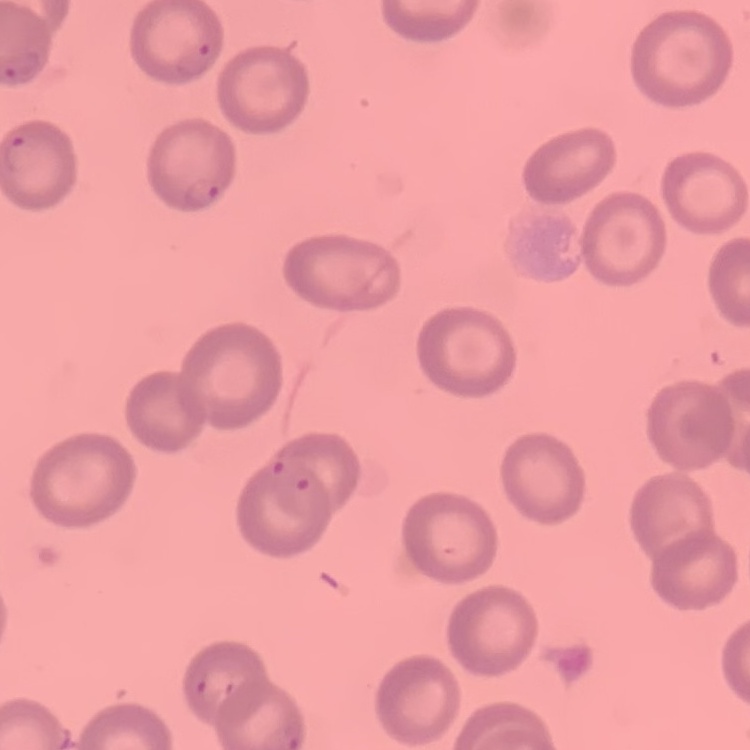 The erythrocytes exhibit no rouleaux formation. One tile cut from a larger photomicrograph. Field's or Giemsa stain. Thin blood film.